Assess this cell for malaria.
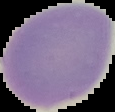
It is uninfected.

image type = segmented cell region with the area outside set to black
preparation = thin blood film
image size = 115×112 pixels